Report the malaria status of this cell.
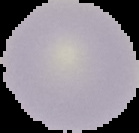

It is uninfected.

Summary:
  - Preparation: thin blood smear
  - Image type: segmented cell region on a black background
  - Image size: 139×133 pixels